State which cell type is depicted.
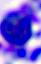
This is a leukocyte.

modality = micrograph
magnification = 400x